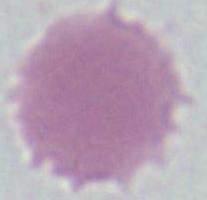
Micrograph. A red blood cell is shown. Captured at 1000x magnification.